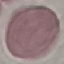
{
  "result": "negative for malaria parasites",
  "image_type": "automatically extracted cell patch, resized to 64 × 64 pixels",
  "preparation": "thin blood film",
  "capture": "smartphone camera at the microscope eyepiece",
  "stain": "Giemsa"
}